Assess this cell for malaria.
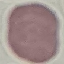

It is uninfected.

capture = smartphone camera at the microscope eyepiece
stain = Giemsa
preparation = thin smear
image type = cell patch, automatically extracted from a larger field of view and resized to 64 × 64 pixels